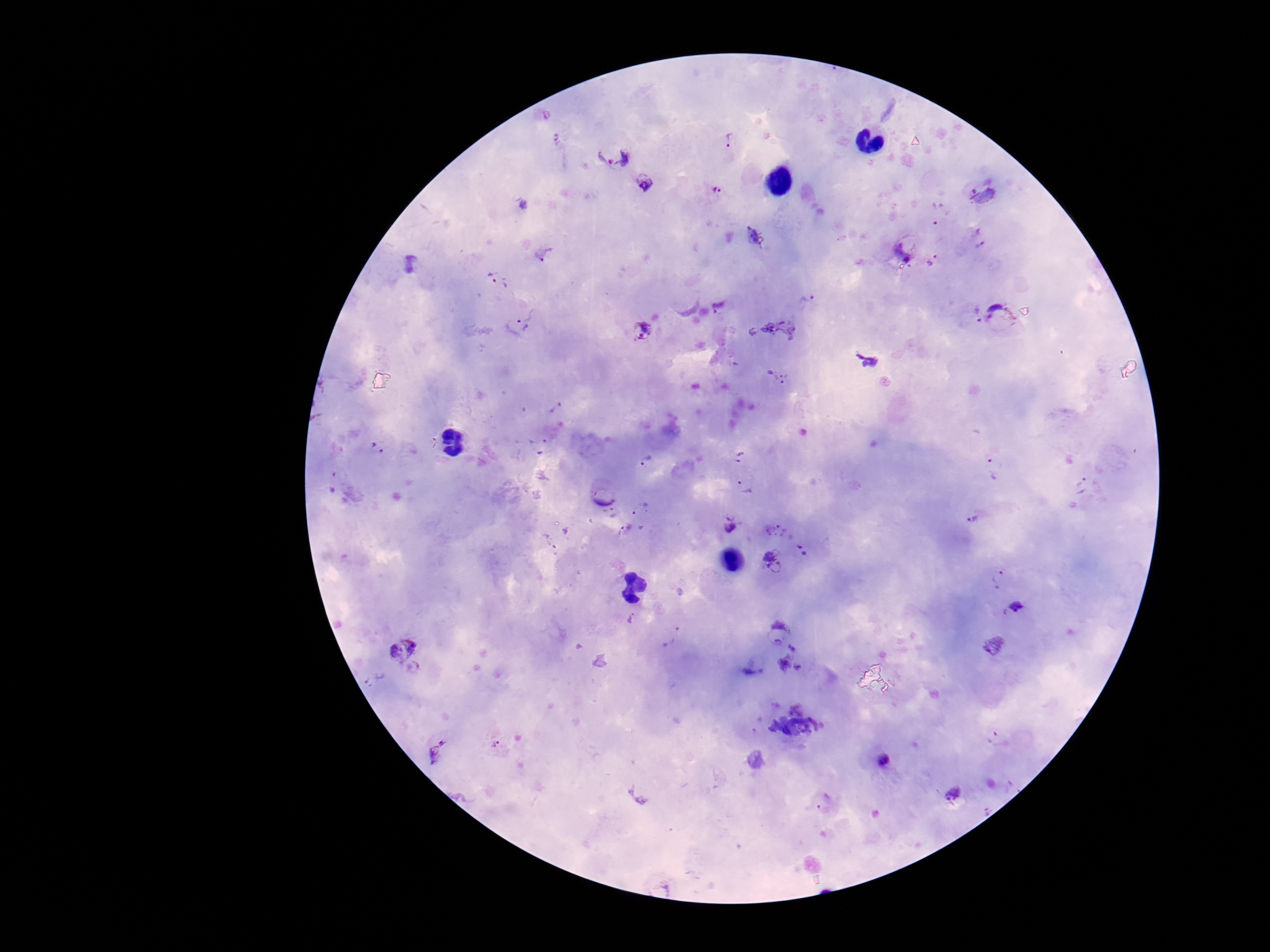

Approximate centers as (x, y) in pixels.
Summary:
  - Plasmodium parasite locations: (548, 116), (558, 139), (729, 139), (613, 153), (645, 182), (716, 190), (983, 191), (940, 214), (756, 236), (909, 249), (546, 256), (934, 263), (500, 280), (808, 301), (720, 305), (970, 315), (1000, 315), (524, 325), (644, 331), (776, 377), (537, 445), (378, 449), (741, 457), (649, 462), (994, 467), (332, 482), (744, 484), (1082, 484), (642, 509), (612, 515), (977, 516), (729, 522), (774, 530), (624, 532), (803, 549), (772, 561), (999, 577), (1012, 607), (632, 619), (780, 631), (668, 634), (995, 647), (403, 649), (793, 662), (375, 681), (998, 740), (497, 744), (437, 752), (884, 760), (956, 793), (826, 804)
  - Stain: Giemsa
  - Field of view: one from this slide
  - Magnification: 100x
  - Preparation: thick blood smear
  - Image size: 1270×952 pixels
  - Capture: smartphone camera through the microscope eyepiece
  - Patient malaria status: positive